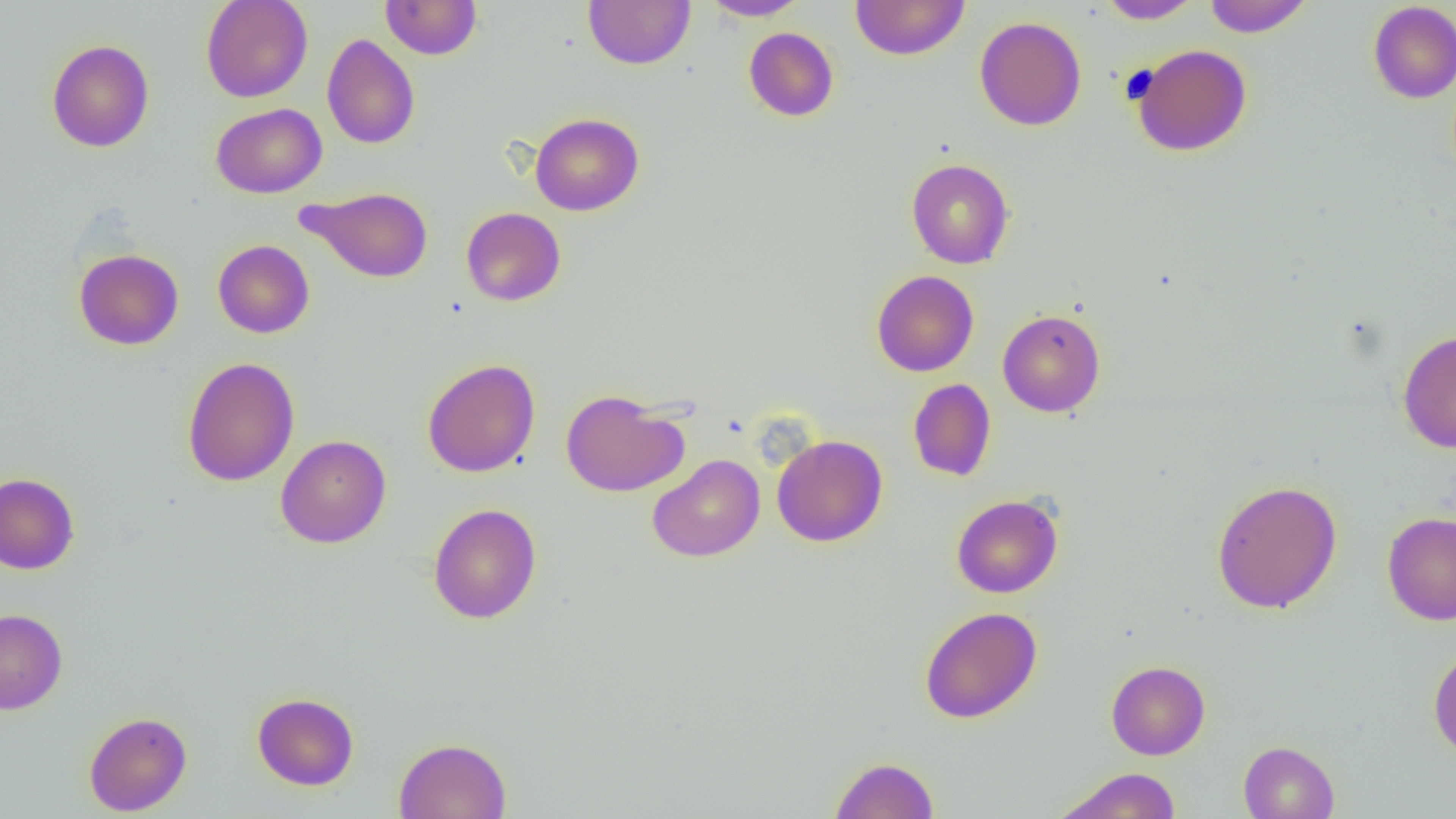

Approximate bounding boxes as (x1, y1, x2, y2) in pixels. Uninfected red blood cell locations: (201, 0, 313, 102), (380, 0, 482, 60), (583, 0, 695, 69), (700, 0, 809, 20), (850, 0, 969, 60), (1096, 0, 1203, 24), (1203, 0, 1312, 37), (1368, 1, 1456, 104), (974, 16, 1087, 131), (743, 27, 839, 122), (321, 34, 420, 149), (46, 39, 155, 153), (1131, 44, 1252, 156), (210, 103, 327, 198), (530, 113, 644, 216), (906, 158, 1014, 269), (299, 186, 434, 283), (461, 207, 566, 307), (212, 240, 314, 338), (73, 248, 184, 350), (871, 270, 979, 377), (997, 309, 1105, 417), (1397, 329, 1456, 453), (181, 357, 300, 487), (422, 358, 540, 478), (908, 378, 996, 481), (561, 390, 688, 496), (275, 434, 391, 548), (772, 434, 888, 547), (648, 454, 765, 562), (0, 472, 80, 574), (1211, 479, 1342, 614), (951, 493, 1064, 598), (428, 503, 542, 624), (1382, 511, 1456, 626), (920, 606, 1042, 724), (0, 608, 68, 714), (1428, 645, 1456, 760), (1106, 660, 1210, 760), (252, 692, 359, 791), (84, 711, 192, 816), (393, 738, 512, 819), (1238, 740, 1339, 819), (830, 756, 939, 818), (1055, 768, 1182, 819). Slide-level diagnosis: negative for blood parasites. Optical microscopy. One field of a larger specimen. Captured at 1000x magnification. Image is 1456×819 pixels. Thin blood film.